Assess this cell for malaria.
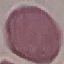

It is uninfected.

image type = automatically extracted cell patch, resized to 64 × 64 pixels
preparation = thin blood smear
capture = smartphone through the microscope eyepiece
stain = Giemsa